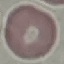
Result: no malaria parasites detected. Acquired by smartphone through the microscope eyepiece. Thin blood smear. Giemsa stain. Cell patch, automatically extracted from a larger field of view and resized to 64 × 64 pixels.